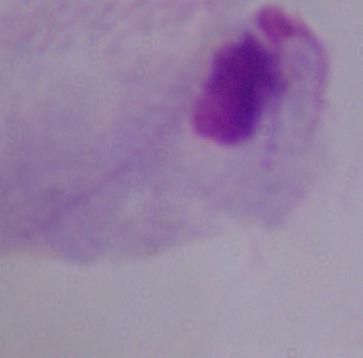
identification = trichomonad
magnification = 1000x
modality = micrograph